Describe the morphology of the red blood cells.
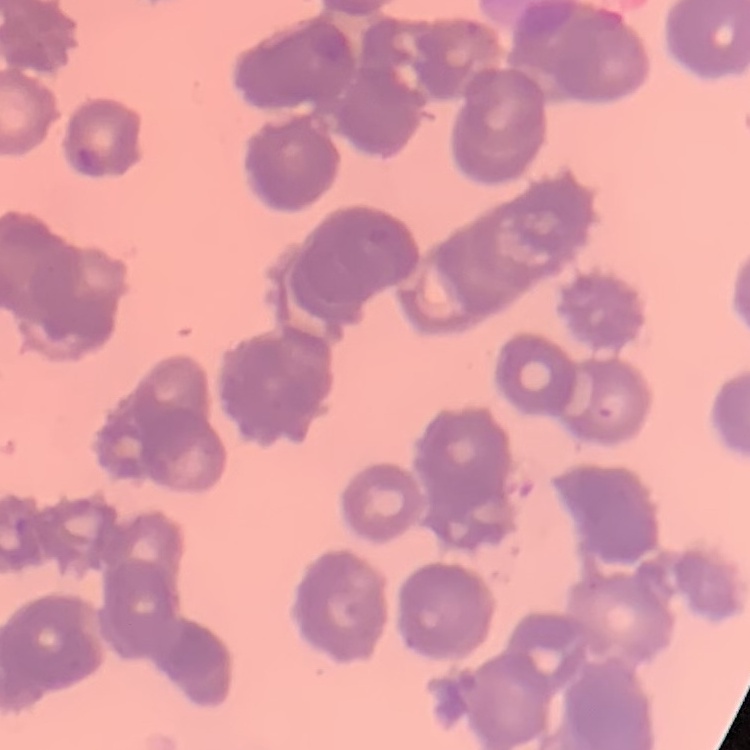

They show rouleaux formation.

Thin peripheral smear. One tile cut from a larger photomicrograph. Stained with either Field's or Giemsa.